Comment on the morphology of the red blood cells.
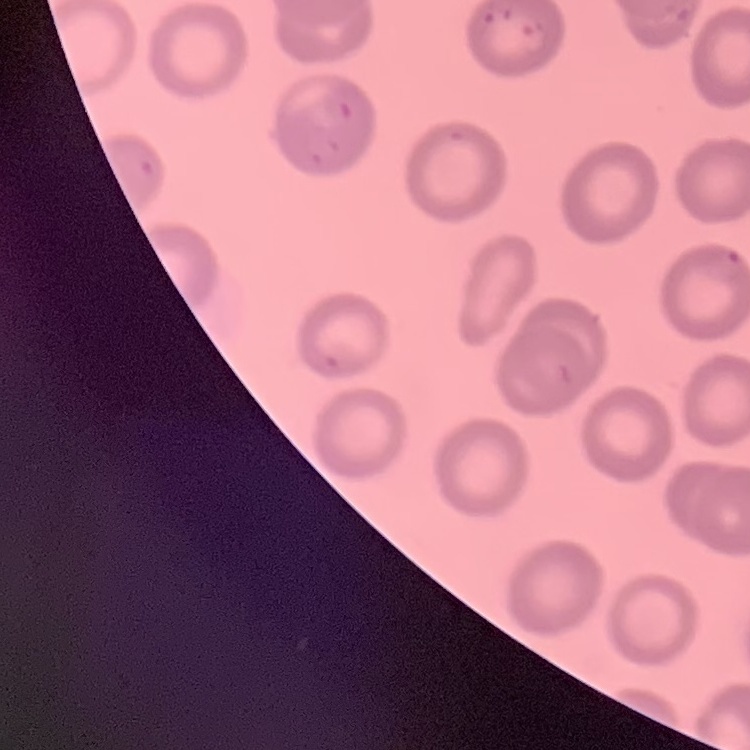

No rouleaux formation.

Field's or Giemsa stain. Thin blood film. Square crop of a larger photomicrograph.